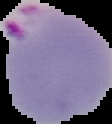
{
  "image_type": "segmented cell region on a black background",
  "malaria_status": "parasitized",
  "preparation": "thin blood smear",
  "image_size": "112×124 pixels"
}